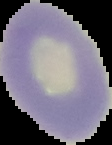

Summary:
  - Preparation: thin blood film
  - Image size: 112×145 pixels
  - Malaria status: uninfected
  - Image type: segmented cell region on a black background